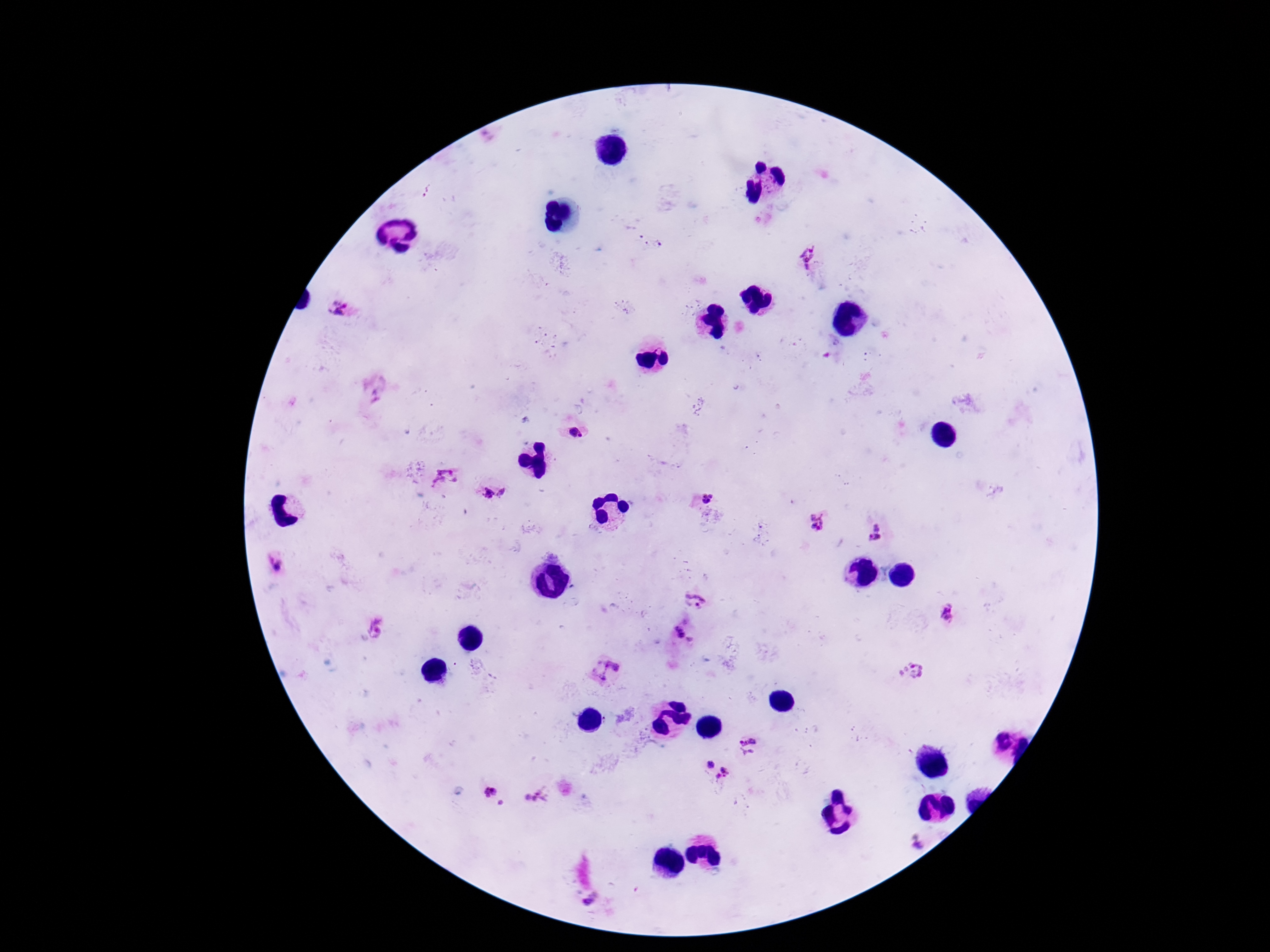 Approximate object centers, in pixels from the top-left corner. Plasmodium parasite locations: (x=427, y=191), (x=649, y=239), (x=807, y=255), (x=338, y=308), (x=576, y=434), (x=443, y=478), (x=487, y=493), (x=502, y=493), (x=707, y=497), (x=817, y=523), (x=875, y=534), (x=277, y=567), (x=696, y=599), (x=948, y=615), (x=380, y=628), (x=684, y=632), (x=604, y=669), (x=912, y=672), (x=749, y=746), (x=710, y=765), (x=724, y=777), (x=490, y=791), (x=535, y=798), (x=504, y=804), (x=918, y=842), (x=591, y=902). Photographed through the microscope eyepiece with a smartphone camera. Patient malaria status: positive. Image is 1270×952 pixels. 100x magnification. Giemsa-stained preparation. One field from this slide. Thick blood smear.